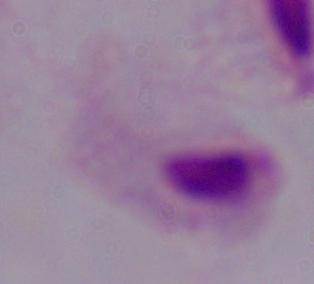
Micrograph. A trichomonad is seen. Captured at 1000x magnification.